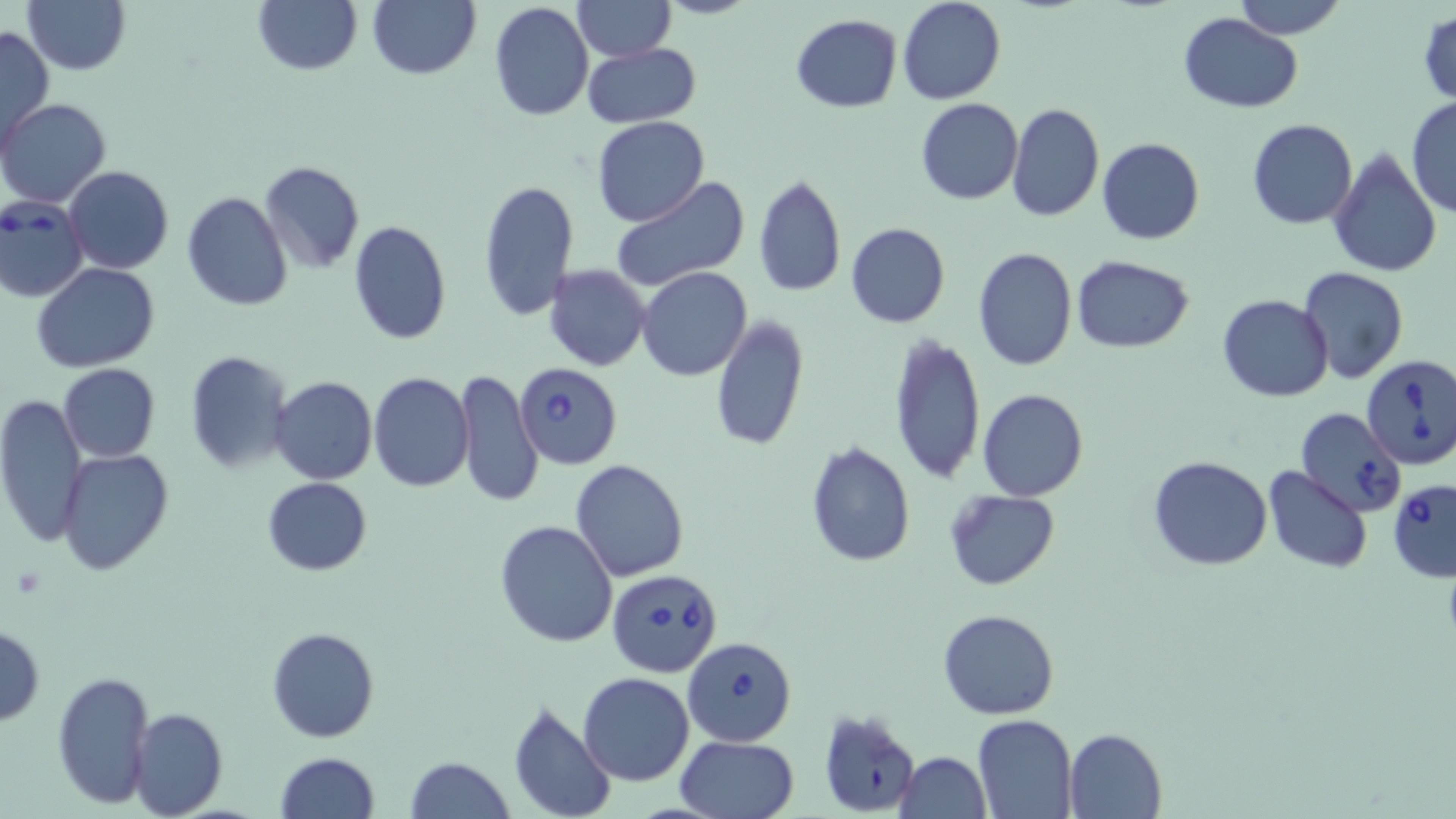

{
  "slide_level_diagnosis": "Babesia divergens",
  "preparation": "thin blood smear",
  "stain": "May-Grünwald-Giemsa",
  "modality": "light microscopy",
  "magnification": "1000x",
  "field_of_view": "one of a larger specimen",
  "image_size": "1456×819 pixels",
  "babesia_divergens_infected_red_blood_cell_locations": "approximate bounding boxes as (x1,y1)-(x2,y2) corner pairs in pixels: (0,193)-(90,303), (1360,354)-(1456,469), (515,363)-(623,469), (1295,408)-(1407,517), (1388,478)-(1456,582), (607,568)-(723,677), (684,636)-(796,746)",
  "uninfected_red_blood_cell_locations": "approximate bounding boxes as (x1,y1)-(x2,y2) corner pairs in pixels: (23,0)-(131,75), (251,0)-(363,76), (367,0)-(481,80), (572,0)-(674,62), (897,0)-(1005,105), (1233,0)-(1346,40), (490,2)-(594,121), (1178,11)-(1304,112), (1416,11)-(1456,107), (790,14)-(902,113), (0,26)-(54,150), (582,42)-(701,127), (916,97)-(1023,204), (1405,97)-(1456,219), (1,99)-(111,208), (1006,103)-(1106,223), (592,117)-(710,226), (1248,119)-(1359,230), (1097,137)-(1204,244), (1329,147)-(1441,277), (258,161)-(367,274), (63,166)-(174,274), (753,174)-(846,298), (610,176)-(751,291), (477,178)-(580,322), (182,192)-(294,310), (347,219)-(453,345), (845,222)-(950,328), (973,247)-(1078,370), (1070,254)-(1196,353), (33,263)-(160,371), (544,264)-(652,372), (1299,266)-(1408,384), (638,267)-(750,381), (1217,294)-(1332,402), (710,315)-(809,453), (886,332)-(986,484), (184,350)-(293,473), (59,363)-(160,462), (454,368)-(544,507), (369,373)-(474,492), (271,376)-(377,485), (976,388)-(1088,501), (0,394)-(87,550), (803,441)-(917,569), (56,449)-(174,574), (1148,455)-(1272,569), (570,459)-(690,582), (1265,466)-(1372,574), (262,476)-(372,575), (944,489)-(1060,591), (494,518)-(618,647), (938,609)-(1058,719), (0,626)-(44,724), (266,626)-(379,743), (50,671)-(155,810), (578,673)-(695,786), (507,701)-(617,819), (128,707)-(227,818), (817,708)-(922,816), (973,713)-(1078,818), (1063,728)-(1167,817), (675,735)-(801,819), (275,752)-(380,819), (895,752)-(991,819), (405,756)-(514,819)"
}